Locate the cells, classifying each as a parasitized RBC, an uninfected RBC, or a WBC.
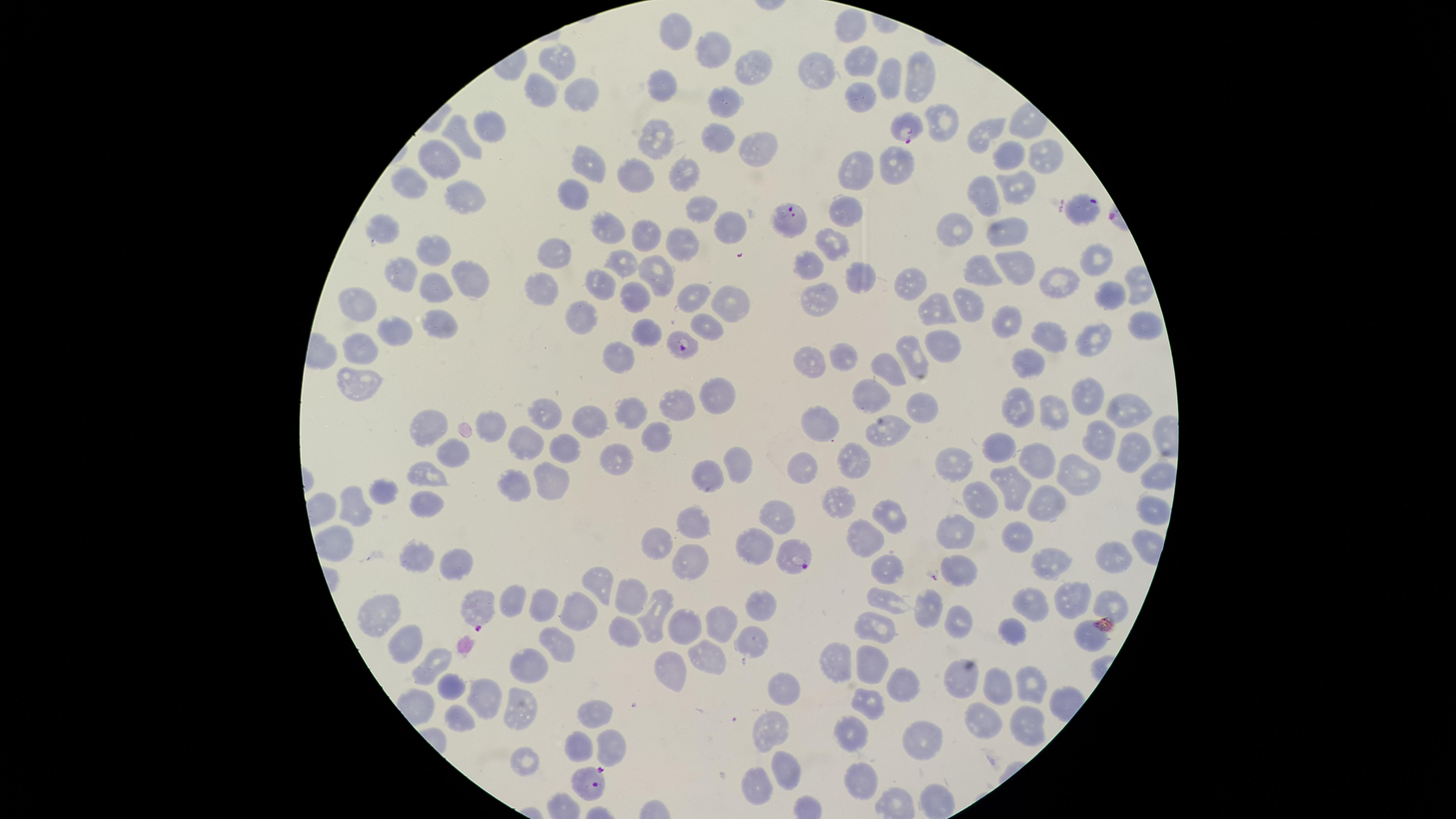

Approximate marker points as (x, y) in pixels.
Parasitized RBCs: (906, 126), (1083, 207), (792, 220), (682, 343), (795, 554), (483, 613), (588, 778).
Uninfected RBCs: (845, 23), (677, 32), (707, 51), (857, 63), (552, 64), (751, 64), (810, 73), (886, 77), (916, 77), (659, 85), (540, 93), (576, 96), (858, 99), (720, 101), (943, 120), (987, 128), (489, 129), (658, 136), (714, 136), (458, 138), (755, 148), (1010, 154), (1045, 155), (892, 158), (437, 161), (592, 165), (636, 170), (856, 170), (682, 174), (1016, 186), (407, 188), (574, 190), (987, 194), (463, 198), (700, 205), (844, 207), (385, 226), (609, 226), (725, 227), (958, 228), (1001, 230), (640, 232), (833, 238), (675, 242), (435, 249), (557, 255), (811, 256), (1095, 256), (617, 262), (1009, 264), (658, 269), (978, 271), (397, 274), (462, 277), (857, 278), (1062, 279), (601, 280), (912, 283), (429, 286), (546, 290), (822, 292), (1111, 292), (634, 296), (689, 296), (728, 300), (974, 301), (357, 302), (943, 310), (438, 317), (587, 318), (1007, 319), (1140, 323), (708, 326), (390, 332), (642, 333), (1095, 337), (1055, 338), (936, 349), (843, 350), (356, 351), (623, 355), (909, 355), (807, 361), (1027, 361), (889, 367), (360, 390), (869, 390), (1087, 396), (716, 397), (920, 401), (678, 403), (1015, 409), (1128, 411), (541, 412), (1054, 413), (630, 415), (427, 419), (584, 421), (487, 424), (821, 424), (886, 424), (1100, 437), (656, 439), (530, 441), (564, 444), (998, 444), (1133, 449), (614, 452), (452, 454), (1032, 454), (855, 459), (951, 461), (808, 463), (732, 466), (1078, 468), (430, 473), (549, 475), (707, 475), (1152, 477), (517, 485), (385, 488), (1007, 490), (982, 496), (424, 503), (840, 503), (360, 507), (1150, 507), (1046, 509), (779, 516), (895, 518), (696, 525), (957, 529), (861, 537), (1014, 539), (656, 544), (751, 551), (1113, 554), (416, 555), (1050, 558), (458, 562), (689, 565), (889, 570), (961, 575), (600, 579), (1078, 597), (517, 598), (887, 600), (546, 603), (630, 604), (1107, 604), (760, 605), (1027, 605), (929, 610), (581, 615), (375, 618), (683, 623), (653, 624), (718, 624), (958, 624), (871, 625), (1016, 630), (1091, 633), (754, 635), (626, 637), (407, 642), (555, 644), (707, 659), (836, 661), (872, 662), (435, 667), (667, 672), (523, 674), (962, 679), (1031, 684), (449, 686), (905, 686), (1000, 688), (485, 690), (790, 696), (872, 701), (520, 711), (600, 712), (463, 719), (1025, 722), (979, 725), (774, 734), (928, 734), (848, 736), (614, 738), (575, 749), (526, 755), (790, 775), (861, 780), (751, 789).
No WBCs identified.

Species: Plasmodium falciparum. Smartphone photograph through the microscope eyepiece. The visible region is circular. Giemsa stain. Image is 1456×819 pixels. Thin blood smear. One field of view of the specimen.